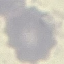
Result: negative for malaria parasites. Automatically extracted cell patch, resized to 64 × 64 pixels. Acquired by smartphone through the microscope eyepiece. Thin smear of blood. Giemsa-stained preparation.